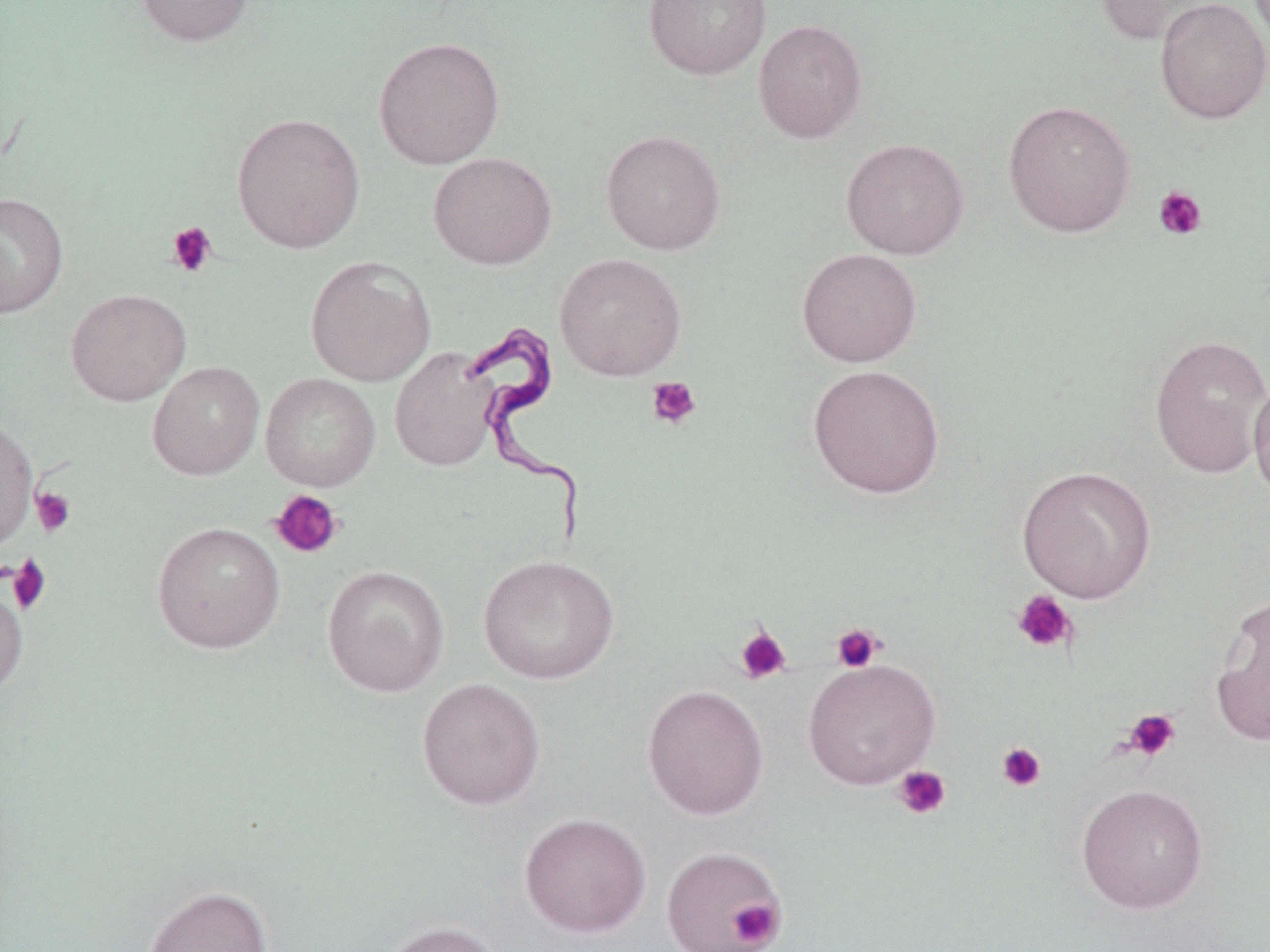

slide-level diagnosis = Trypanosoma brucei
platelet locations (subset) = approximate bounding boxes as named x1/y1/x2/y2 corners in pixels: (x1=1153, y1=185, x2=1208, y2=241), (x1=166, y1=222, x2=217, y2=277), (x1=646, y1=376, x2=702, y2=429), (x1=31, y1=487, x2=76, y2=537), (x1=270, y1=489, x2=343, y2=559), (x1=6, y1=554, x2=52, y2=615), (x1=1011, y1=589, x2=1078, y2=654), (x1=831, y1=623, x2=885, y2=673), (x1=734, y1=624, x2=792, y2=685), (x1=1122, y1=708, x2=1182, y2=761), (x1=996, y1=742, x2=1047, y2=792), (x1=893, y1=766, x2=951, y2=820), (x1=727, y1=897, x2=785, y2=950)
uninfected red blood cell locations (subset) = approximate bounding boxes as named x1/y1/x2/y2 corners in pixels: (x1=134, y1=0, x2=254, y2=46), (x1=643, y1=0, x2=771, y2=80), (x1=1094, y1=0, x2=1225, y2=47), (x1=1154, y1=0, x2=1270, y2=124), (x1=753, y1=19, x2=868, y2=143), (x1=373, y1=36, x2=505, y2=169), (x1=1002, y1=100, x2=1136, y2=237), (x1=231, y1=111, x2=366, y2=254), (x1=600, y1=129, x2=726, y2=255), (x1=841, y1=138, x2=970, y2=259), (x1=428, y1=151, x2=557, y2=270), (x1=0, y1=192, x2=68, y2=318), (x1=797, y1=247, x2=922, y2=367), (x1=554, y1=253, x2=687, y2=381), (x1=305, y1=255, x2=436, y2=386), (x1=66, y1=288, x2=192, y2=406), (x1=1149, y1=334, x2=1270, y2=479), (x1=389, y1=346, x2=501, y2=472), (x1=147, y1=360, x2=265, y2=480), (x1=807, y1=363, x2=946, y2=499), (x1=260, y1=372, x2=381, y2=491), (x1=1249, y1=377, x2=1270, y2=504), (x1=0, y1=416, x2=38, y2=552), (x1=1017, y1=465, x2=1157, y2=603), (x1=152, y1=520, x2=285, y2=653), (x1=478, y1=554, x2=619, y2=684), (x1=322, y1=564, x2=450, y2=697), (x1=0, y1=579, x2=29, y2=700), (x1=1210, y1=592, x2=1270, y2=748), (x1=416, y1=678, x2=546, y2=810), (x1=641, y1=684, x2=770, y2=820), (x1=1075, y1=783, x2=1210, y2=914), (x1=518, y1=812, x2=652, y2=938), (x1=142, y1=885, x2=273, y2=952), (x1=381, y1=920, x2=503, y2=952)
modality = light microscopy
Trypanosoma brucei locations = approximate bounding boxes as named x1/y1/x2/y2 corners in pixels: (x1=461, y1=316, x2=591, y2=555)
preparation = thin blood film
image size = 1270×952 pixels
field of view = one of a larger specimen
magnification = 1000x
stain = May-Grünwald-Giemsa